Name the cell type shown.
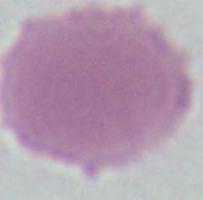
This is an erythrocyte.

modality: photomicrograph
magnification: 1000x